State which cell type is depicted.
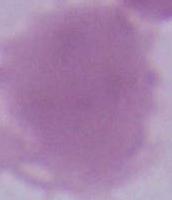

An erythrocyte.

Summary:
  - Magnification: 1000x
  - Modality: photomicrograph